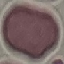 Result: no malaria parasites detected. Giemsa stain. Cell patch, automatically extracted from a larger field of view and resized to 64 × 64 pixels. Photographed with a smartphone camera at the microscope eyepiece. Thin smear of blood.